Give the position of every Plasmodium parasite.
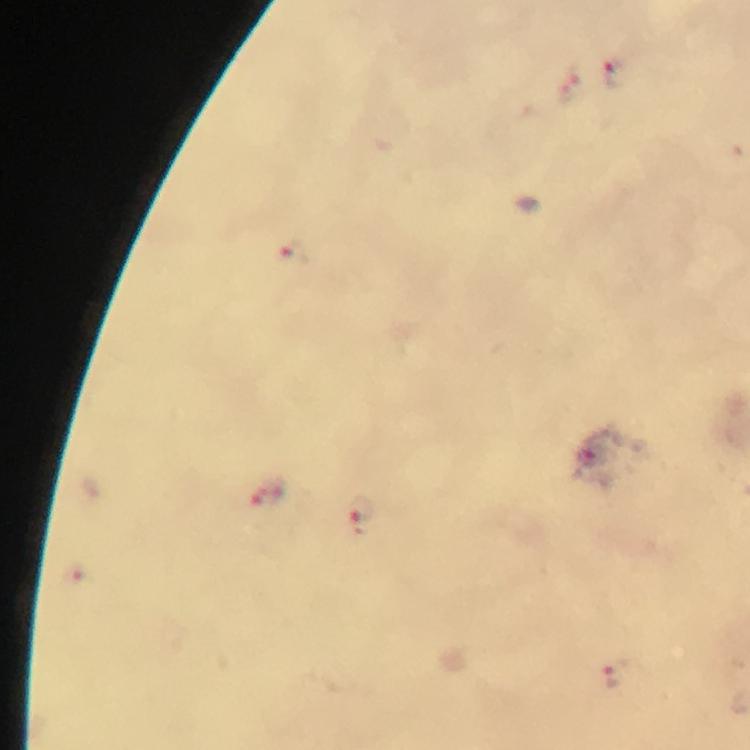
Approximate centers as (x, y) in pixels.
Plasmodium parasites: (615, 73), (293, 253), (593, 455), (268, 495), (360, 513), (618, 675).

Summary:
  - Stain: Giemsa
  - Image size: 750×750 pixels
  - Magnification: 100x
  - Cropped from: one field of view
  - Context: from a malaria diagnostic workup
  - Preparation: thick blood film
  - Immersion oil: used
  - Capture: smartphone camera through the microscope